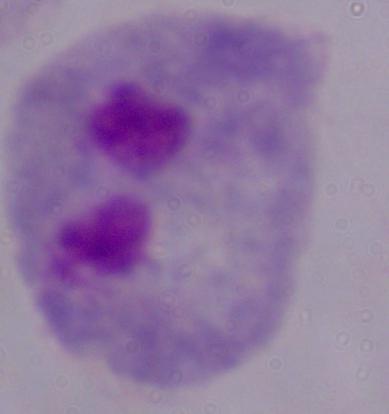

Captured at 1000x magnification. A trichomonad is shown. Micrograph.